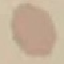

Malaria status: uninfected. Giemsa-stained preparation. Photographed with a smartphone camera at the microscope eyepiece. Automatically extracted cell patch, resized to 64 × 64 pixels. Thin blood smear.